Describe the morphology of the red blood cells.
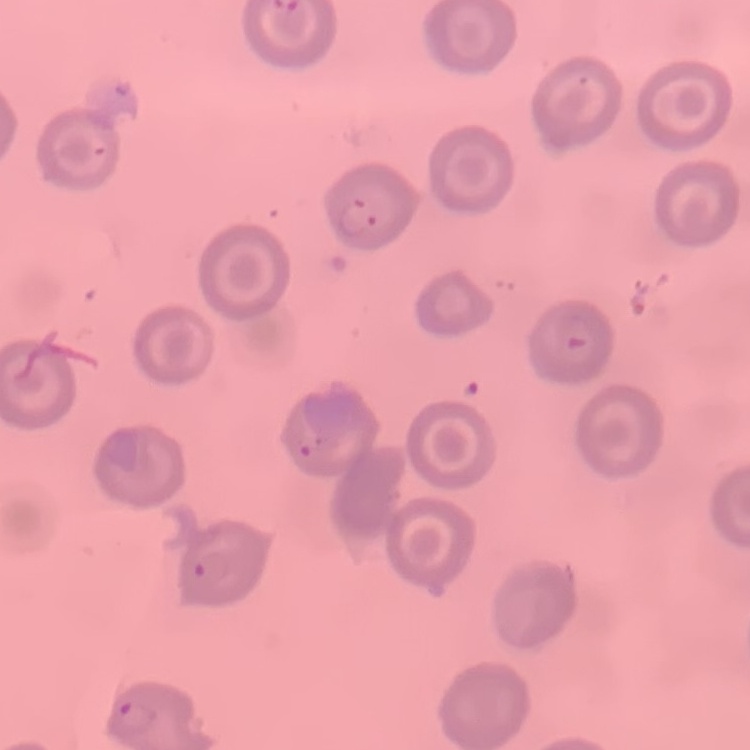

No rouleaux formation.

image_type: one tile cut from a larger photomicrograph
stain: Field's or Giemsa
preparation: thin blood film